Name the parasite shown.
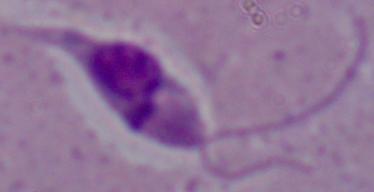
This is Leishmania.

{
  "modality": "micrograph",
  "magnification": "1000x"
}